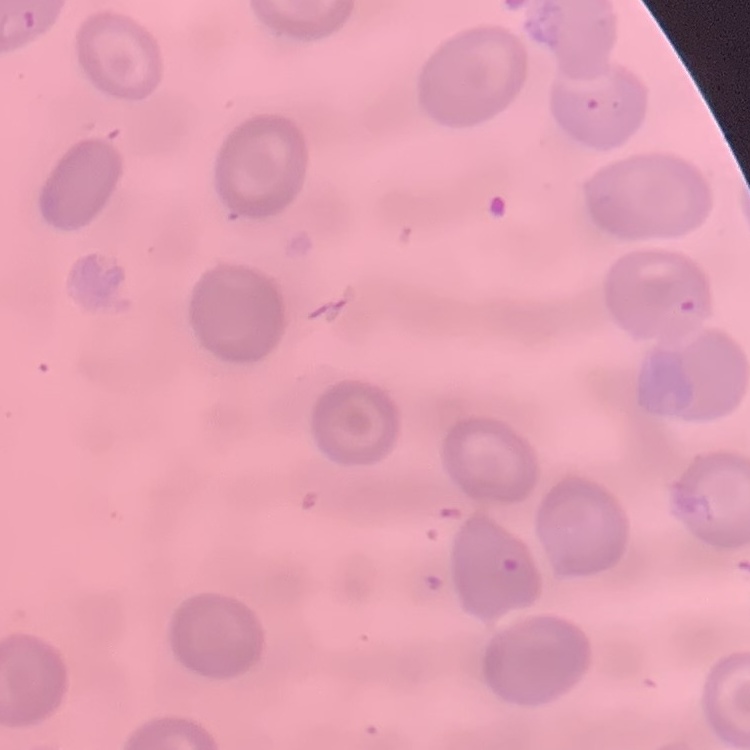

red blood cell morphology = no rouleaux formation
stain = Field's or Giemsa
image type = square crop of a larger photomicrograph
preparation = thin blood film